Name the cell type shown.
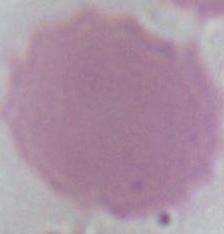

An erythrocyte.

Summary:
  - Magnification: 1000x
  - Modality: photomicrograph